Identify the parasite.
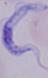
A trypanosome.

modality = micrograph
magnification = 1000x